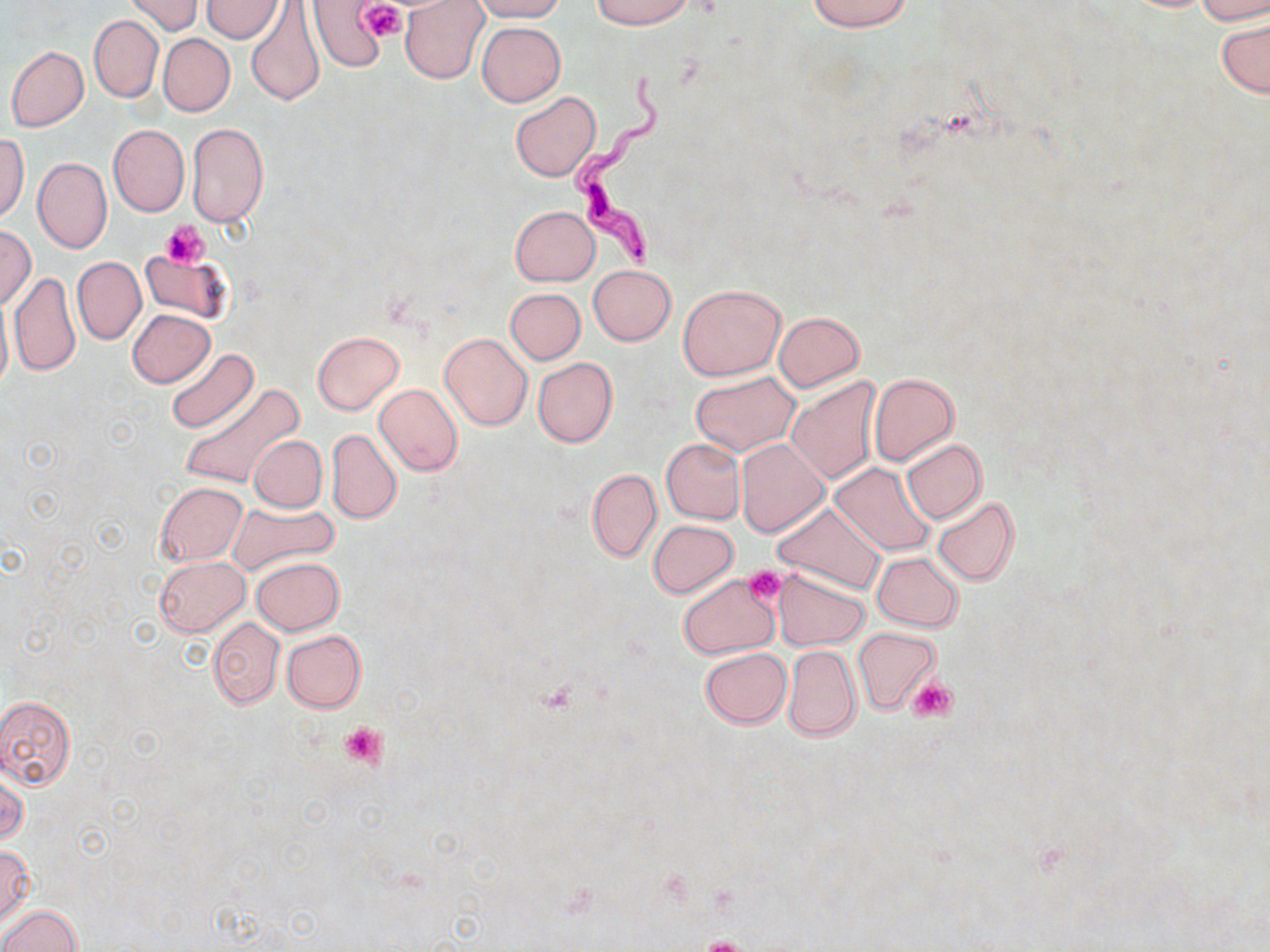 Approximate bounding boxes as named x1/y1/x2/y2 corners in pixels. Uninfected red blood cell locations: (x1=125, y1=0, x2=201, y2=36), (x1=245, y1=0, x2=326, y2=105), (x1=308, y1=0, x2=390, y2=72), (x1=400, y1=0, x2=490, y2=85), (x1=469, y1=0, x2=566, y2=21), (x1=590, y1=0, x2=692, y2=28), (x1=807, y1=0, x2=912, y2=32), (x1=1193, y1=0, x2=1270, y2=25), (x1=203, y1=1, x2=282, y2=42), (x1=89, y1=15, x2=163, y2=102), (x1=1218, y1=17, x2=1269, y2=98), (x1=477, y1=22, x2=565, y2=106), (x1=158, y1=33, x2=235, y2=116), (x1=6, y1=46, x2=89, y2=132), (x1=511, y1=91, x2=601, y2=182), (x1=187, y1=123, x2=268, y2=228), (x1=108, y1=124, x2=189, y2=217), (x1=0, y1=134, x2=29, y2=223), (x1=32, y1=156, x2=112, y2=254), (x1=509, y1=205, x2=600, y2=286), (x1=0, y1=226, x2=36, y2=309), (x1=139, y1=249, x2=230, y2=323), (x1=72, y1=257, x2=145, y2=344), (x1=589, y1=264, x2=676, y2=345), (x1=8, y1=273, x2=81, y2=377), (x1=678, y1=283, x2=785, y2=380), (x1=504, y1=288, x2=586, y2=365), (x1=0, y1=293, x2=12, y2=396), (x1=128, y1=309, x2=214, y2=387), (x1=773, y1=311, x2=865, y2=390), (x1=312, y1=331, x2=404, y2=415), (x1=438, y1=333, x2=533, y2=431), (x1=166, y1=347, x2=257, y2=434), (x1=533, y1=358, x2=617, y2=447), (x1=690, y1=371, x2=800, y2=454), (x1=869, y1=373, x2=959, y2=465), (x1=784, y1=377, x2=882, y2=485), (x1=179, y1=384, x2=304, y2=490), (x1=373, y1=384, x2=463, y2=476), (x1=326, y1=428, x2=401, y2=523), (x1=247, y1=435, x2=327, y2=512), (x1=661, y1=438, x2=746, y2=524), (x1=901, y1=438, x2=987, y2=525), (x1=736, y1=439, x2=828, y2=537), (x1=831, y1=463, x2=936, y2=556), (x1=587, y1=468, x2=662, y2=563), (x1=155, y1=482, x2=247, y2=565), (x1=931, y1=497, x2=1020, y2=587), (x1=226, y1=501, x2=338, y2=575), (x1=773, y1=502, x2=884, y2=594), (x1=649, y1=520, x2=738, y2=598), (x1=872, y1=551, x2=964, y2=632), (x1=155, y1=556, x2=248, y2=635), (x1=251, y1=556, x2=344, y2=635), (x1=773, y1=569, x2=869, y2=650), (x1=679, y1=574, x2=780, y2=659), (x1=208, y1=617, x2=285, y2=708), (x1=853, y1=627, x2=940, y2=714), (x1=281, y1=630, x2=366, y2=713), (x1=782, y1=645, x2=860, y2=741), (x1=700, y1=648, x2=792, y2=728), (x1=0, y1=696, x2=75, y2=788), (x1=0, y1=770, x2=27, y2=847), (x1=0, y1=847, x2=33, y2=926), (x1=1, y1=905, x2=81, y2=952). Platelet locations: (x1=360, y1=2, x2=406, y2=42), (x1=162, y1=222, x2=208, y2=268), (x1=742, y1=564, x2=786, y2=606), (x1=907, y1=677, x2=955, y2=721), (x1=339, y1=720, x2=387, y2=768), (x1=695, y1=938, x2=757, y2=952). Trypanosoma brucei locations: (x1=573, y1=66, x2=669, y2=270). Slide-level diagnosis: Trypanosoma brucei. Image is 1270×952 pixels. Captured at 1000x magnification. Optical microscopy. May-Grünwald-Giemsa stain. One field of a larger specimen. Thin blood film.